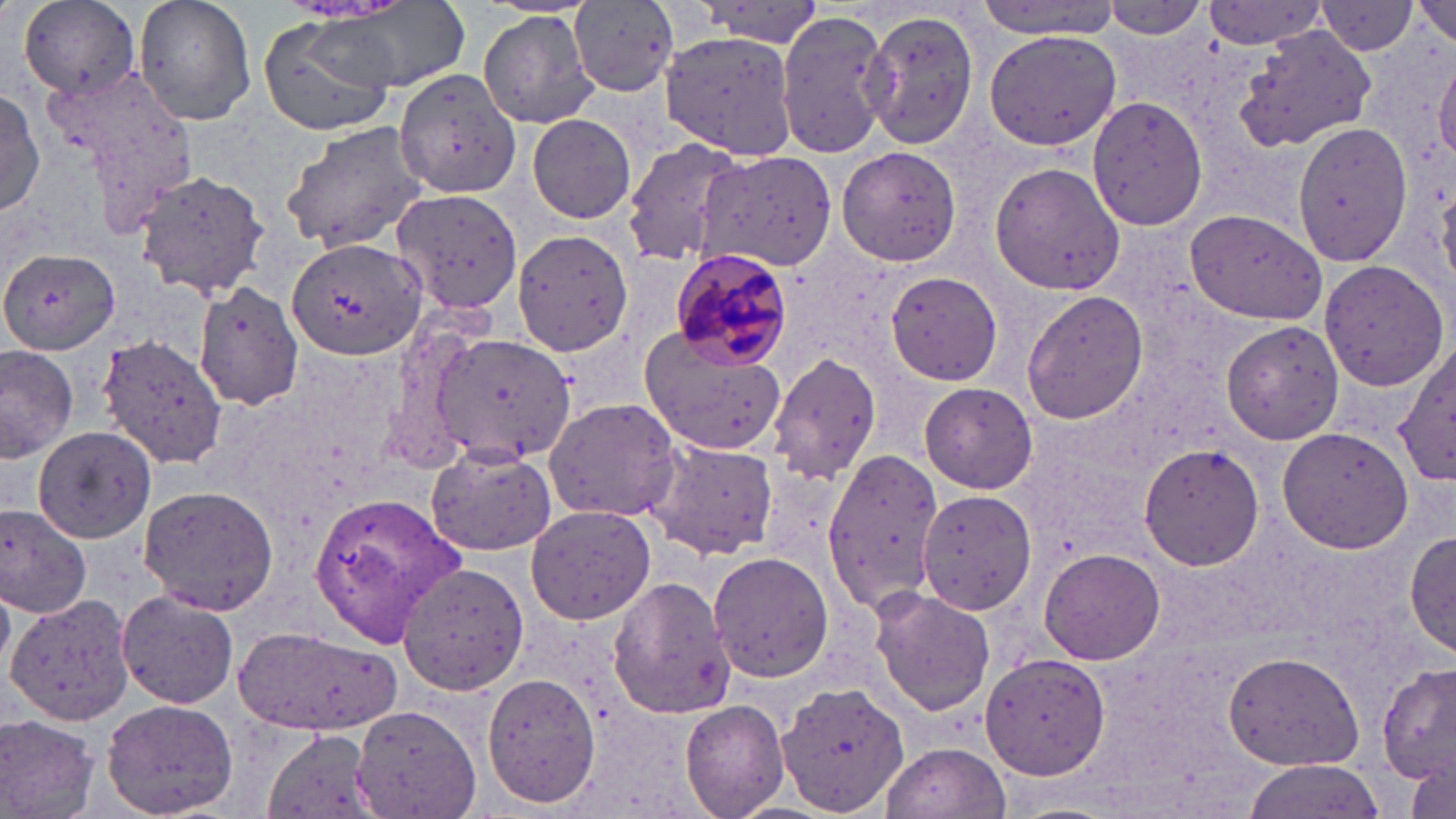
slide-level diagnosis = Plasmodium malariae
magnification = 1000x
modality = optical microscopy
preparation = thin blood smear
image size = 1456×819 pixels
Plasmodium malariae-infected red blood cell locations = approximate bounding boxes as (x1, y1, x2, y2) in pixels: (667, 249, 796, 372)
uninfected red blood cell locations = approximate bounding boxes as (x1, y1, x2, y2) in pixels: (131, 0, 258, 128), (974, 0, 1121, 38), (1412, 0, 1456, 47), (19, 1, 142, 104), (1099, 1, 1212, 47), (294, 2, 471, 96), (563, 2, 679, 97), (1199, 3, 1332, 50), (1316, 3, 1420, 55), (477, 8, 598, 129), (861, 8, 980, 147), (775, 9, 891, 162), (254, 13, 408, 138), (982, 26, 1122, 153), (1235, 27, 1376, 152), (659, 28, 800, 162), (1433, 55, 1456, 166), (40, 59, 198, 231), (394, 67, 520, 200), (0, 87, 45, 219), (1086, 96, 1208, 229), (526, 112, 639, 225), (1292, 119, 1413, 268), (278, 120, 430, 251), (620, 136, 746, 267), (834, 144, 961, 266), (695, 151, 837, 271), (988, 162, 1128, 296), (130, 168, 271, 299), (391, 189, 523, 315), (1185, 209, 1327, 323), (510, 227, 638, 356), (285, 236, 425, 363), (0, 248, 121, 353), (1316, 257, 1451, 393), (886, 270, 1003, 385), (196, 280, 304, 409), (1021, 290, 1148, 424), (1220, 318, 1345, 445), (639, 326, 788, 458), (97, 333, 229, 468), (432, 333, 574, 467), (1397, 342, 1456, 486), (0, 345, 78, 461), (767, 353, 881, 483), (918, 382, 1036, 493), (544, 397, 680, 523), (1277, 426, 1414, 554), (34, 427, 155, 541), (647, 439, 777, 560), (1139, 443, 1265, 570), (428, 446, 556, 556), (822, 451, 944, 625), (138, 484, 278, 613), (306, 488, 466, 646), (917, 490, 1037, 614), (525, 503, 656, 625), (0, 505, 93, 618), (1406, 528, 1456, 661), (1040, 546, 1166, 664), (708, 549, 833, 683), (397, 561, 529, 696), (607, 573, 736, 723), (116, 587, 237, 709), (869, 587, 996, 717), (4, 593, 133, 725), (237, 624, 403, 739), (1223, 649, 1367, 772), (981, 652, 1112, 779), (1378, 663, 1454, 785), (482, 673, 601, 808), (776, 681, 910, 817), (102, 699, 239, 816), (680, 700, 791, 819), (354, 702, 482, 819), (0, 713, 100, 819), (264, 728, 380, 818), (881, 741, 1009, 819), (1404, 754, 1455, 819), (1242, 762, 1385, 819)
stain = May-Grünwald-Giemsa
field of view = single